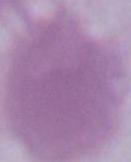 Captured at 1000x magnification. An erythrocyte is shown. Micrograph.